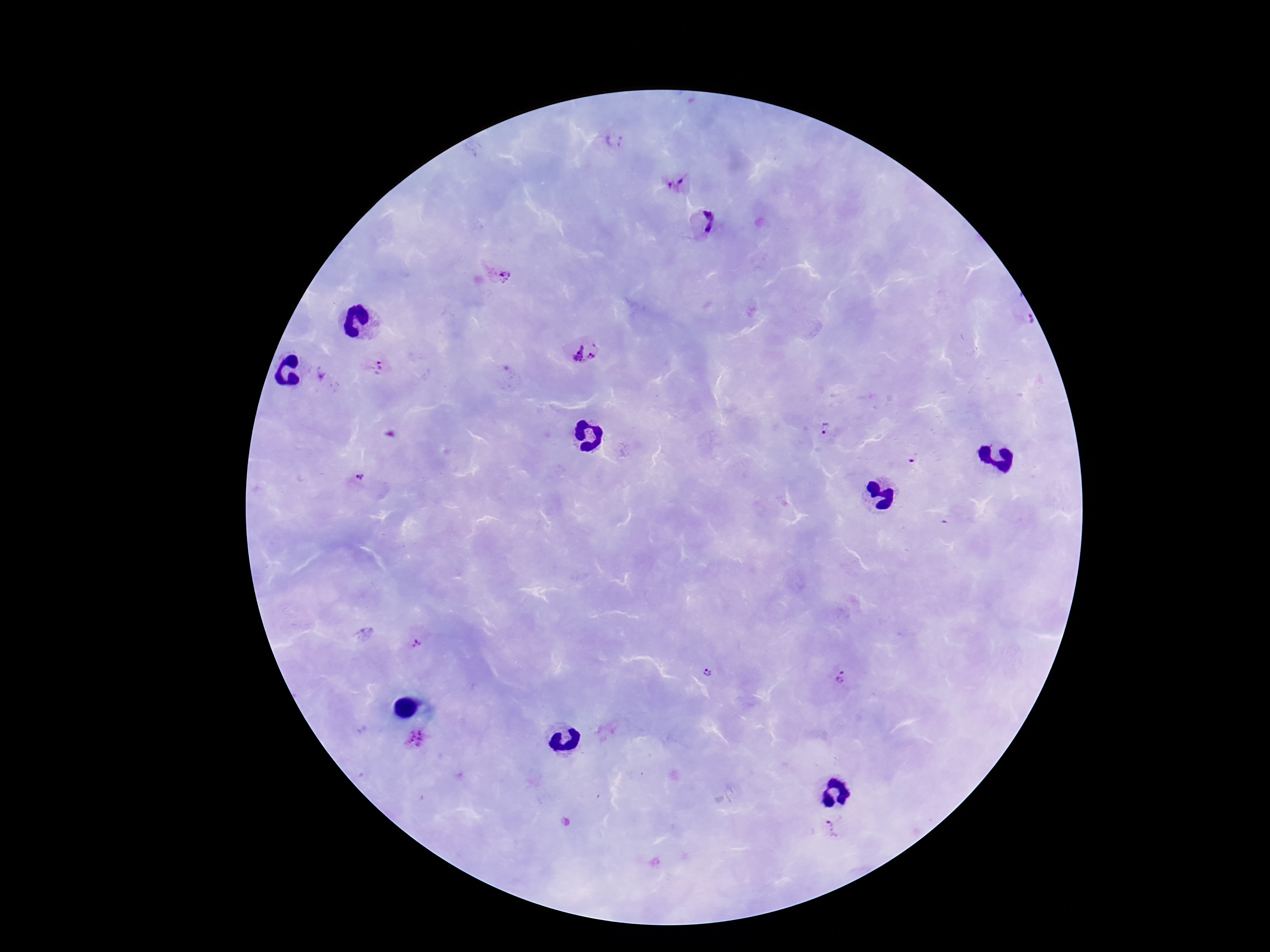

capture: smartphone camera through the microscope eyepiece
field_of_view: one from this slide
plasmodium_parasite_locations: 'approximate object centers, in pixels from the top-left corner: (x=616, y=142), (x=678, y=185), (x=703, y=223), (x=501, y=274), (x=571, y=351), (x=593, y=355), (x=377, y=365), (x=321, y=374), (x=824, y=429), (x=913, y=458), (x=361, y=478), (x=415, y=644), (x=709, y=673), (x=842, y=678), (x=415, y=739), (x=833, y=827)'
patient_malaria_status: positive
stain: Giemsa
preparation: thick blood film
image_size: 1270×952 pixels
magnification: 100x